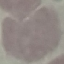

result = negative for malaria parasites
stain = Giemsa
image type = cell patch, automatically extracted from a larger field of view and resized to 64 × 64 pixels
capture = smartphone through the microscope eyepiece
preparation = thin smear